Locate every blood parasite and identify its species.
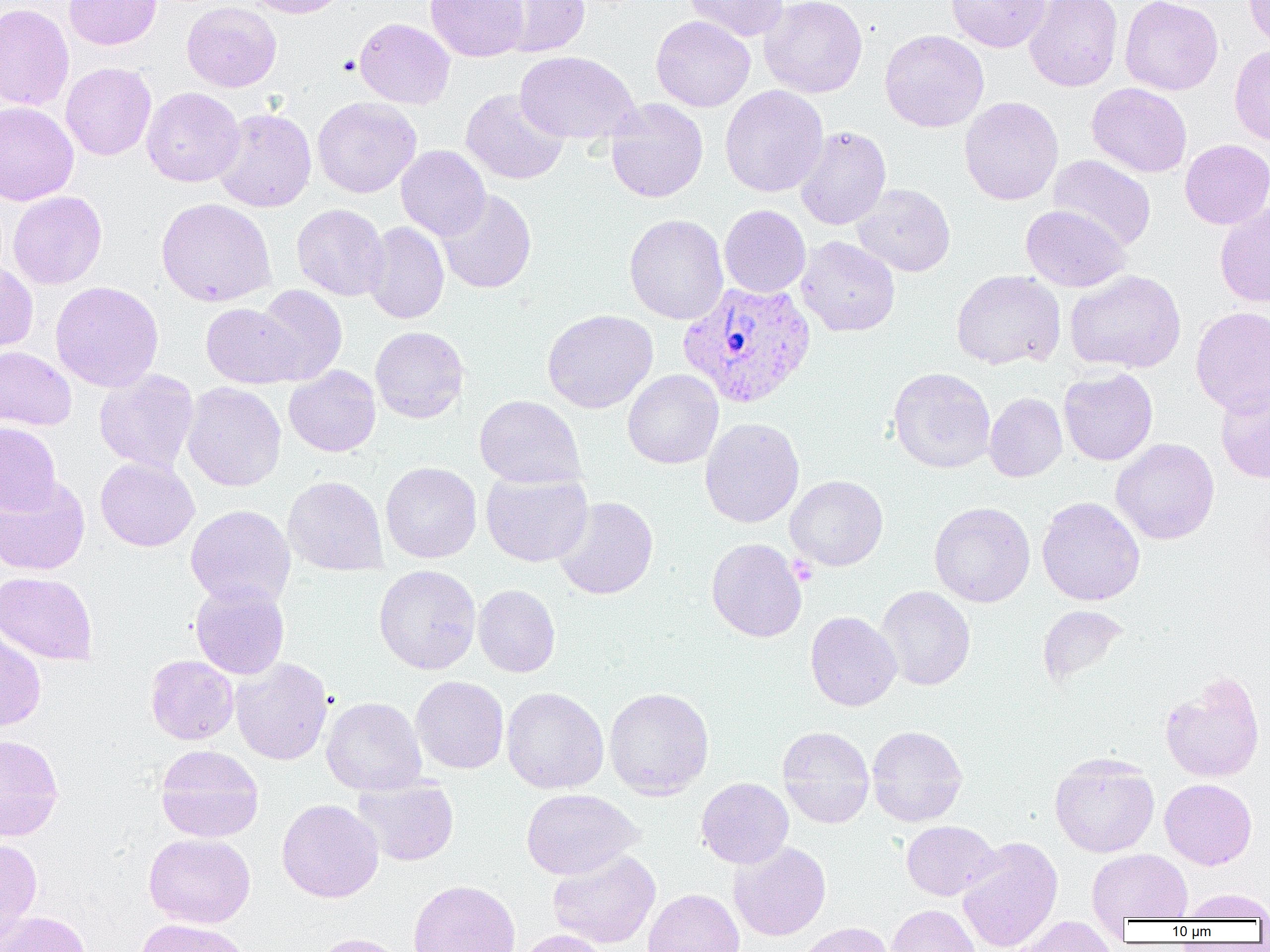

Approximate bounding boxes as named x1/y1/x2/y2 corners in pixels.
Plasmodium vivax-infected red blood cells: (x1=678, y1=281, x2=817, y2=409).
No Plasmodium falciparum, Plasmodium ovale, Plasmodium malariae, Babesia divergens, or Trypanosoma brucei observed.

Summary:
  - Platelet locations: (x1=788, y1=555, x2=817, y2=586)
  - Uninfected red blood cell locations: (x1=64, y1=0, x2=162, y2=50), (x1=243, y1=0, x2=351, y2=18), (x1=426, y1=0, x2=529, y2=62), (x1=486, y1=0, x2=591, y2=58), (x1=683, y1=0, x2=789, y2=42), (x1=759, y1=0, x2=867, y2=98), (x1=946, y1=0, x2=1050, y2=53), (x1=1024, y1=0, x2=1123, y2=92), (x1=1120, y1=0, x2=1223, y2=95), (x1=1243, y1=0, x2=1270, y2=51), (x1=181, y1=2, x2=282, y2=92), (x1=0, y1=3, x2=75, y2=111), (x1=651, y1=16, x2=755, y2=112), (x1=354, y1=18, x2=454, y2=109), (x1=879, y1=29, x2=989, y2=132), (x1=1229, y1=44, x2=1270, y2=146), (x1=515, y1=51, x2=639, y2=144), (x1=61, y1=63, x2=156, y2=160), (x1=1087, y1=83, x2=1192, y2=178), (x1=720, y1=85, x2=828, y2=197), (x1=141, y1=87, x2=245, y2=187), (x1=461, y1=89, x2=569, y2=185), (x1=960, y1=96, x2=1063, y2=205), (x1=312, y1=97, x2=421, y2=198), (x1=605, y1=99, x2=708, y2=202), (x1=0, y1=101, x2=79, y2=205), (x1=212, y1=107, x2=316, y2=212), (x1=795, y1=126, x2=891, y2=230), (x1=1180, y1=139, x2=1270, y2=229), (x1=396, y1=145, x2=491, y2=240), (x1=1048, y1=154, x2=1156, y2=252), (x1=852, y1=184, x2=956, y2=277), (x1=436, y1=189, x2=536, y2=294), (x1=7, y1=191, x2=107, y2=289), (x1=156, y1=197, x2=276, y2=307), (x1=1214, y1=202, x2=1270, y2=308), (x1=292, y1=204, x2=389, y2=301), (x1=719, y1=204, x2=810, y2=297), (x1=1021, y1=205, x2=1130, y2=292), (x1=624, y1=214, x2=729, y2=325), (x1=362, y1=221, x2=449, y2=324), (x1=796, y1=236, x2=900, y2=336), (x1=0, y1=258, x2=38, y2=355), (x1=1064, y1=269, x2=1186, y2=374), (x1=951, y1=270, x2=1065, y2=370), (x1=50, y1=281, x2=164, y2=392), (x1=252, y1=285, x2=347, y2=385), (x1=201, y1=303, x2=304, y2=389), (x1=1191, y1=307, x2=1270, y2=415), (x1=542, y1=309, x2=658, y2=413), (x1=370, y1=326, x2=469, y2=423), (x1=0, y1=346, x2=77, y2=431), (x1=284, y1=366, x2=381, y2=457), (x1=888, y1=367, x2=996, y2=474), (x1=1059, y1=368, x2=1158, y2=466), (x1=623, y1=369, x2=723, y2=469), (x1=94, y1=370, x2=199, y2=473), (x1=182, y1=382, x2=286, y2=492), (x1=1216, y1=383, x2=1270, y2=484), (x1=984, y1=392, x2=1067, y2=482), (x1=475, y1=394, x2=585, y2=489), (x1=700, y1=417, x2=804, y2=528), (x1=0, y1=422, x2=61, y2=516), (x1=1111, y1=438, x2=1220, y2=544), (x1=95, y1=456, x2=200, y2=552), (x1=380, y1=461, x2=482, y2=563), (x1=481, y1=472, x2=593, y2=567), (x1=283, y1=475, x2=388, y2=576), (x1=785, y1=475, x2=888, y2=571), (x1=0, y1=476, x2=90, y2=576), (x1=552, y1=496, x2=658, y2=600), (x1=1037, y1=496, x2=1145, y2=605), (x1=929, y1=502, x2=1035, y2=607), (x1=185, y1=504, x2=296, y2=608), (x1=706, y1=538, x2=807, y2=642), (x1=374, y1=565, x2=481, y2=674), (x1=0, y1=570, x2=98, y2=665), (x1=191, y1=581, x2=290, y2=679), (x1=473, y1=584, x2=560, y2=677), (x1=876, y1=586, x2=975, y2=690), (x1=1037, y1=604, x2=1129, y2=687), (x1=805, y1=610, x2=902, y2=711), (x1=0, y1=625, x2=46, y2=732), (x1=145, y1=655, x2=239, y2=745), (x1=230, y1=657, x2=333, y2=765), (x1=1160, y1=669, x2=1266, y2=783), (x1=411, y1=675, x2=508, y2=774), (x1=501, y1=687, x2=609, y2=794), (x1=604, y1=687, x2=714, y2=800), (x1=321, y1=696, x2=427, y2=795), (x1=867, y1=725, x2=968, y2=826), (x1=777, y1=726, x2=875, y2=828), (x1=0, y1=733, x2=64, y2=842), (x1=155, y1=744, x2=264, y2=843), (x1=1050, y1=754, x2=1159, y2=858), (x1=353, y1=777, x2=459, y2=866), (x1=696, y1=777, x2=794, y2=868), (x1=1159, y1=778, x2=1257, y2=870), (x1=521, y1=788, x2=642, y2=880), (x1=276, y1=799, x2=384, y2=902), (x1=901, y1=821, x2=999, y2=901), (x1=143, y1=833, x2=256, y2=928), (x1=957, y1=836, x2=1063, y2=952), (x1=0, y1=837, x2=43, y2=948), (x1=729, y1=841, x2=831, y2=941), (x1=547, y1=849, x2=661, y2=949), (x1=1087, y1=849, x2=1192, y2=923), (x1=408, y1=880, x2=521, y2=952), (x1=642, y1=888, x2=744, y2=952), (x1=1178, y1=888, x2=1270, y2=921), (x1=886, y1=904, x2=982, y2=952), (x1=0, y1=911, x2=91, y2=952), (x1=1013, y1=917, x2=1119, y2=951), (x1=134, y1=918, x2=254, y2=952), (x1=792, y1=921, x2=897, y2=952), (x1=514, y1=929, x2=612, y2=952), (x1=310, y1=933, x2=412, y2=952)
  - Slide-level diagnosis: Plasmodium vivax
  - Field of view: single
  - Modality: optical microscopy
  - Image size: 1270×952 pixels
  - Preparation: thin blood smear
  - Magnification: 1000x